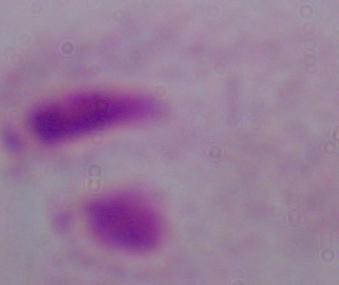

Summary:
  - Identification: trichomonad
  - Modality: photomicrograph
  - Magnification: 1000x